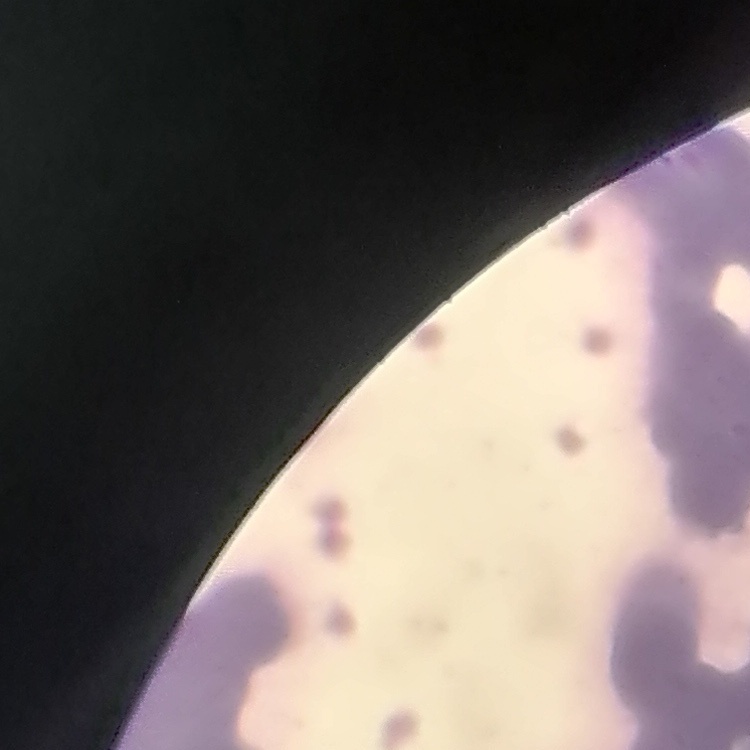

erythrocyte_morphology: rouleaux formation
preparation: thin blood film
stain: Field's or Giemsa
image_type: square crop of a larger photomicrograph